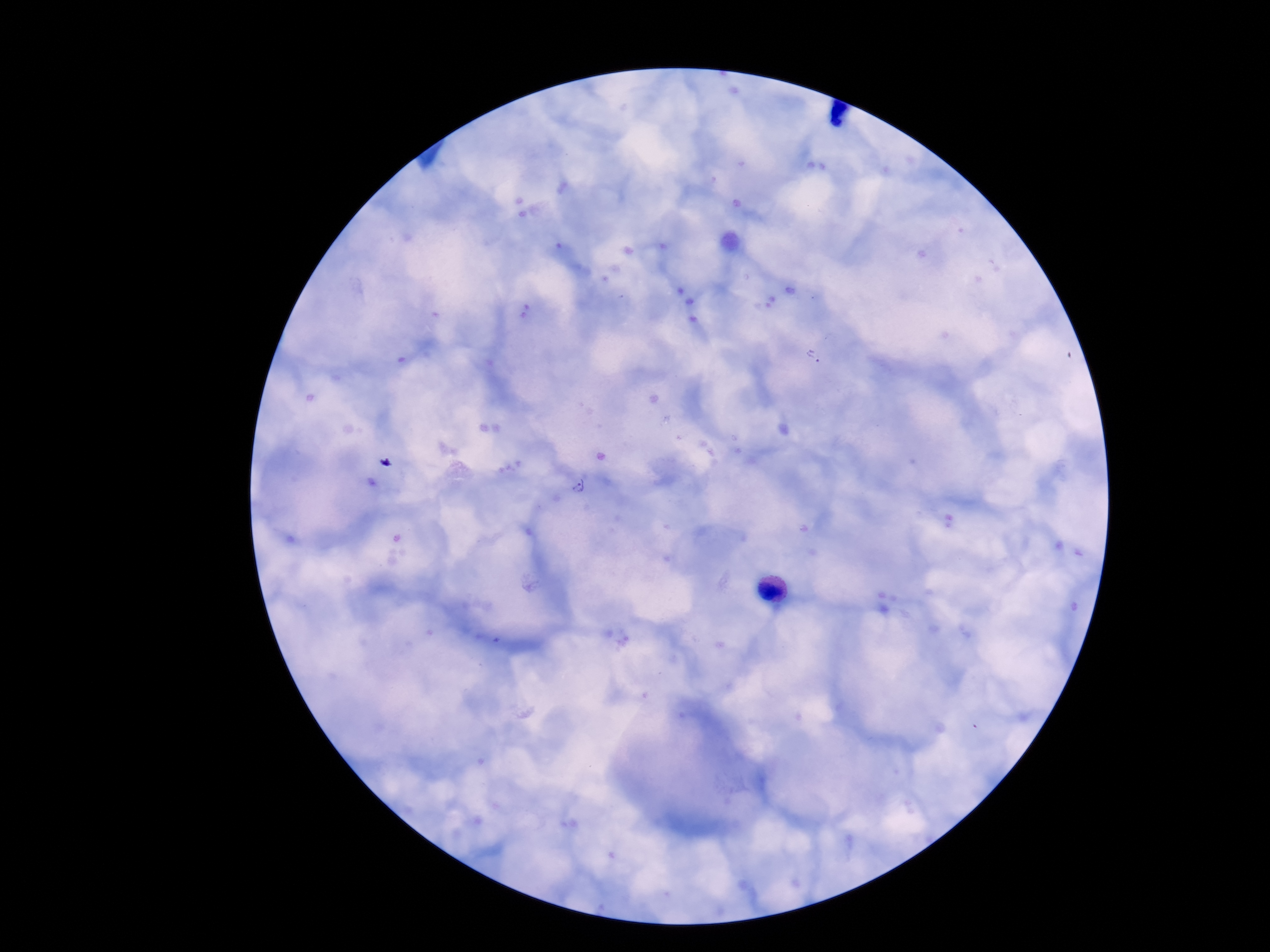
Approximate centers as (x, y) in pixels.
Summary:
  - Plasmodium parasite locations: (812, 355), (580, 485)
  - Magnification: 100x
  - Image size: 1270×952 pixels
  - Preparation: thick peripheral-blood smear
  - Field of view: one from this slide
  - Patient malaria status: infected
  - Stain: Giemsa
  - Capture: smartphone camera through the microscope eyepiece